Assess this cell for malaria.
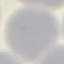
It is uninfected.

preparation = thin blood film
image type = automatically extracted cell patch, resized to 64 × 64 pixels
stain = Giemsa
capture = smartphone camera at the microscope eyepiece